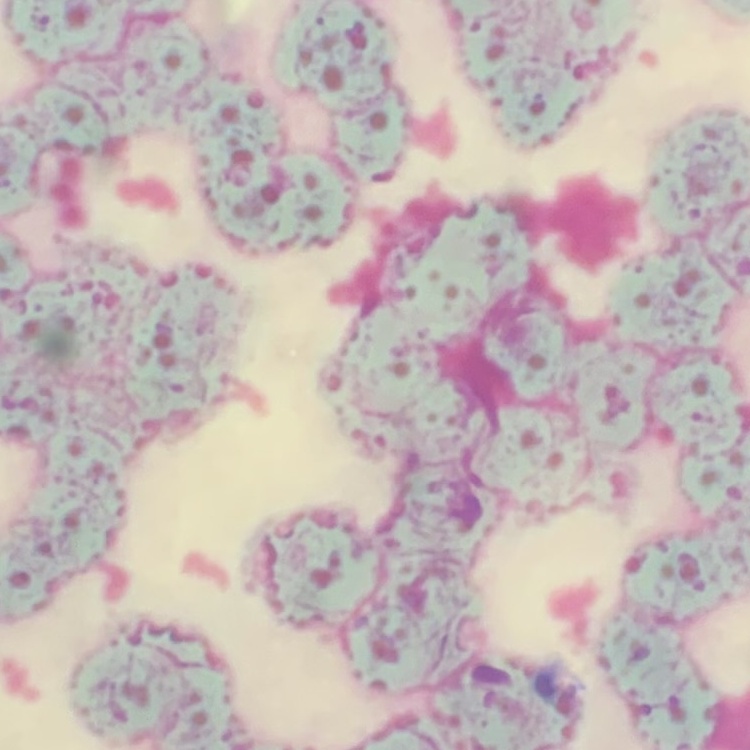
Summary:
  - Erythrocyte morphology: rouleaux formation
  - Preparation: thin peripheral smear
  - Stain: Field's or Giemsa
  - Image type: one tile cut from a larger photomicrograph